Locate every Plasmodium parasite.
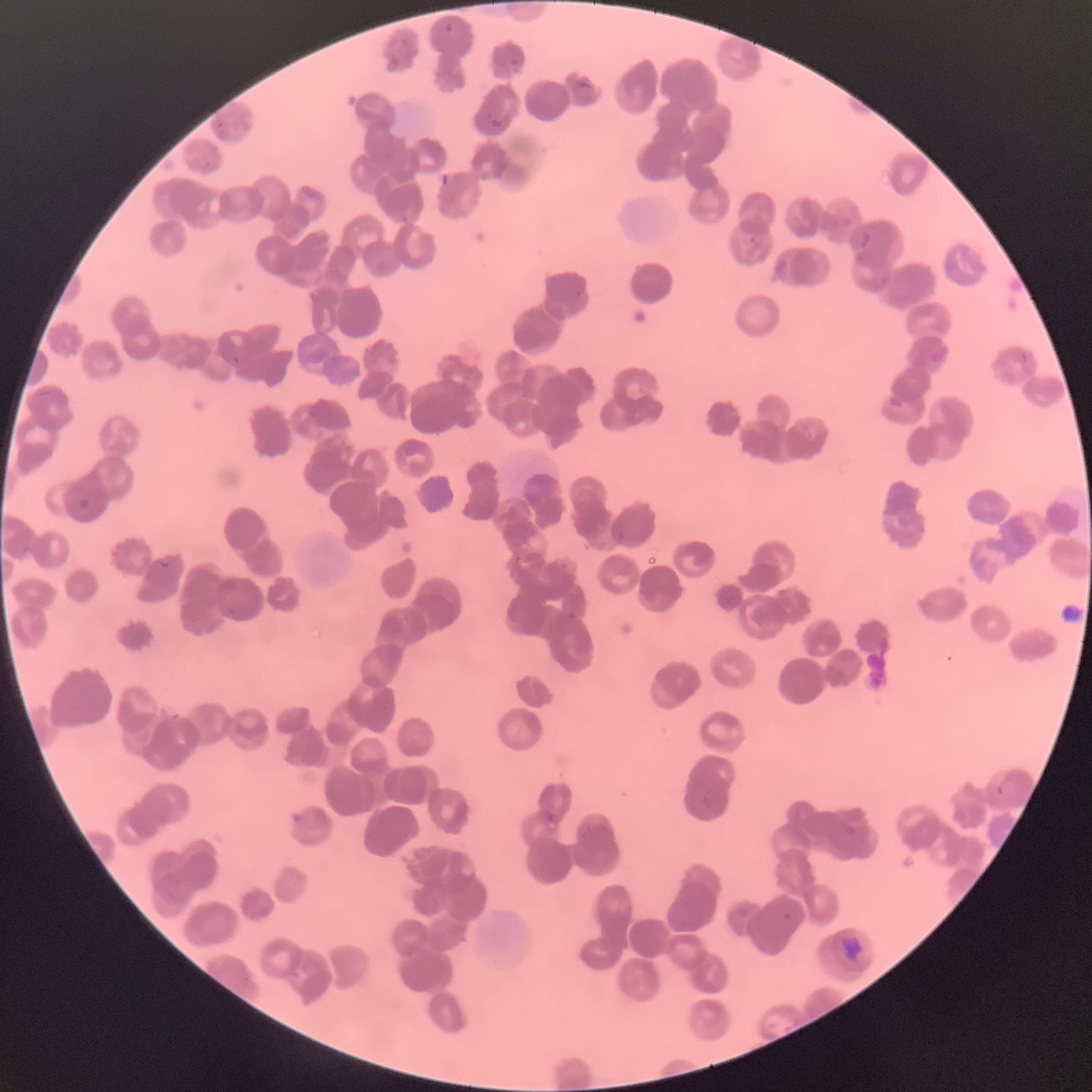

Approximate bounding boxes as (x1,y1)-(x2,y2) corner pairs in pixels.
Plasmodium parasites: (567,611)-(578,620), (996,786)-(1004,795).

Summary:
  - Red blood cell morphology: rouleaux formation
  - Preparation: thin blood film
  - Image size: 1092×1092 pixels
  - Modality: light microscopy